Outline each blood parasite and name the species.
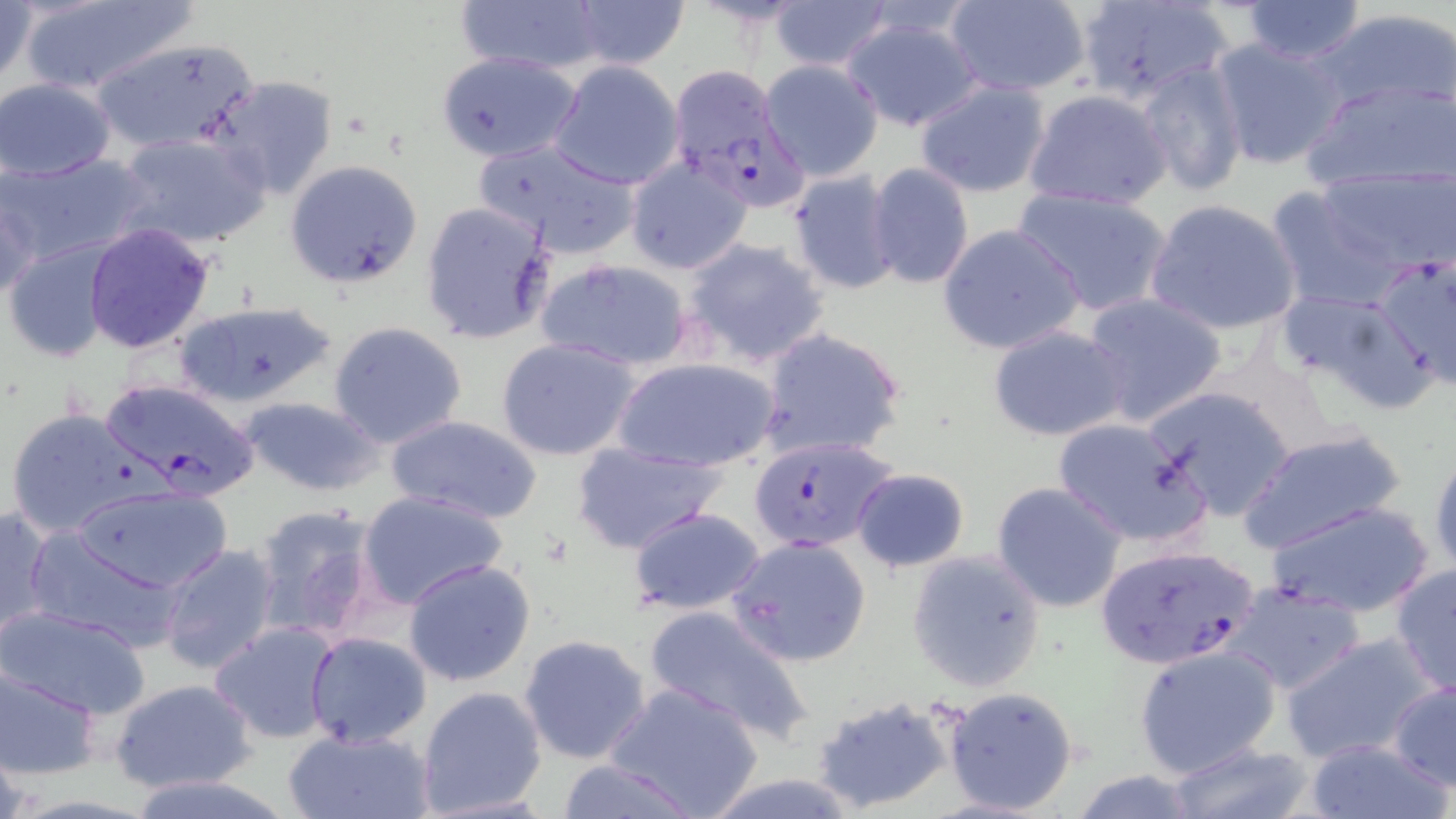

Approximate bounding boxes as named x1/y1/x2/y2 corners in pixels.
Plasmodium falciparum-infected red blood cells: (x1=668, y1=65, x2=819, y2=211), (x1=102, y1=377, x2=263, y2=500), (x1=749, y1=435, x2=897, y2=551), (x1=1093, y1=543, x2=1262, y2=670).
No Plasmodium ovale, Plasmodium malariae, Plasmodium vivax, Babesia divergens, or Trypanosoma brucei observed.

Summary:
  - Uninfected red blood cell locations: (x1=16, y1=0, x2=194, y2=96), (x1=457, y1=0, x2=607, y2=76), (x1=567, y1=0, x2=688, y2=70), (x1=1074, y1=0, x2=1236, y2=107), (x1=1239, y1=0, x2=1368, y2=63), (x1=0, y1=1, x2=38, y2=90), (x1=766, y1=1, x2=894, y2=73), (x1=943, y1=1, x2=1091, y2=98), (x1=1311, y1=7, x2=1456, y2=114), (x1=841, y1=14, x2=984, y2=132), (x1=91, y1=35, x2=260, y2=154), (x1=1207, y1=36, x2=1348, y2=170), (x1=436, y1=52, x2=580, y2=163), (x1=548, y1=60, x2=685, y2=189), (x1=761, y1=60, x2=884, y2=180), (x1=1134, y1=61, x2=1249, y2=199), (x1=210, y1=73, x2=338, y2=199), (x1=0, y1=78, x2=118, y2=182), (x1=1300, y1=79, x2=1454, y2=195), (x1=914, y1=80, x2=1050, y2=198), (x1=1023, y1=88, x2=1172, y2=210), (x1=114, y1=133, x2=270, y2=248), (x1=471, y1=138, x2=642, y2=259), (x1=4, y1=153, x2=151, y2=266), (x1=622, y1=155, x2=754, y2=275), (x1=285, y1=159, x2=421, y2=286), (x1=867, y1=162, x2=975, y2=290), (x1=1317, y1=164, x2=1455, y2=276), (x1=789, y1=171, x2=902, y2=294), (x1=1, y1=176, x2=45, y2=303), (x1=1265, y1=185, x2=1405, y2=314), (x1=1013, y1=186, x2=1174, y2=317), (x1=1145, y1=198, x2=1303, y2=337), (x1=420, y1=200, x2=558, y2=345), (x1=83, y1=223, x2=217, y2=355), (x1=937, y1=223, x2=1086, y2=356), (x1=681, y1=236, x2=830, y2=368), (x1=5, y1=238, x2=118, y2=362), (x1=1372, y1=251, x2=1456, y2=390), (x1=535, y1=257, x2=696, y2=372), (x1=1274, y1=289, x2=1402, y2=388), (x1=1081, y1=290, x2=1226, y2=428), (x1=172, y1=299, x2=338, y2=408), (x1=328, y1=322, x2=469, y2=449), (x1=986, y1=325, x2=1134, y2=443), (x1=757, y1=328, x2=907, y2=462), (x1=496, y1=338, x2=641, y2=461), (x1=614, y1=355, x2=780, y2=473), (x1=1144, y1=384, x2=1299, y2=519), (x1=238, y1=396, x2=383, y2=496), (x1=5, y1=406, x2=147, y2=537), (x1=1051, y1=414, x2=1207, y2=547), (x1=388, y1=415, x2=541, y2=526), (x1=1238, y1=428, x2=1406, y2=555), (x1=573, y1=442, x2=726, y2=554), (x1=1428, y1=445, x2=1456, y2=577), (x1=850, y1=466, x2=971, y2=572), (x1=990, y1=481, x2=1130, y2=614), (x1=71, y1=484, x2=232, y2=592), (x1=358, y1=488, x2=510, y2=611), (x1=1266, y1=500, x2=1437, y2=620), (x1=250, y1=503, x2=384, y2=647), (x1=0, y1=504, x2=52, y2=644), (x1=627, y1=506, x2=769, y2=615), (x1=22, y1=526, x2=178, y2=649), (x1=725, y1=535, x2=872, y2=669), (x1=156, y1=542, x2=281, y2=675), (x1=905, y1=550, x2=1046, y2=693), (x1=667, y1=554, x2=856, y2=708), (x1=403, y1=559, x2=535, y2=686), (x1=1389, y1=564, x2=1455, y2=699), (x1=1226, y1=582, x2=1370, y2=696), (x1=644, y1=602, x2=813, y2=745), (x1=0, y1=605, x2=153, y2=719), (x1=210, y1=622, x2=341, y2=743), (x1=304, y1=631, x2=432, y2=748), (x1=517, y1=633, x2=652, y2=764), (x1=1279, y1=635, x2=1443, y2=767), (x1=1134, y1=644, x2=1283, y2=777), (x1=1, y1=666, x2=101, y2=780), (x1=108, y1=676, x2=257, y2=792), (x1=605, y1=681, x2=764, y2=819), (x1=1387, y1=681, x2=1456, y2=789), (x1=415, y1=684, x2=550, y2=817), (x1=940, y1=685, x2=1077, y2=815), (x1=811, y1=694, x2=956, y2=815), (x1=281, y1=725, x2=434, y2=819), (x1=0, y1=728, x2=30, y2=819), (x1=1299, y1=737, x2=1452, y2=819), (x1=1158, y1=741, x2=1322, y2=819), (x1=553, y1=759, x2=704, y2=817), (x1=698, y1=773, x2=863, y2=818), (x1=126, y1=776, x2=295, y2=819)
  - Slide-level diagnosis: Plasmodium falciparum
  - Field of view: single
  - Modality: light microscopy
  - Preparation: thin blood smear
  - Stain: May-Grünwald-Giemsa
  - Image size: 1456×819 pixels
  - Magnification: 1000x